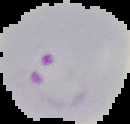

Image is 130×124 pixels. Malaria status: parasitized. From a thin blood smear. Cell region segmented out of the field of view; the surrounding area is masked to black.